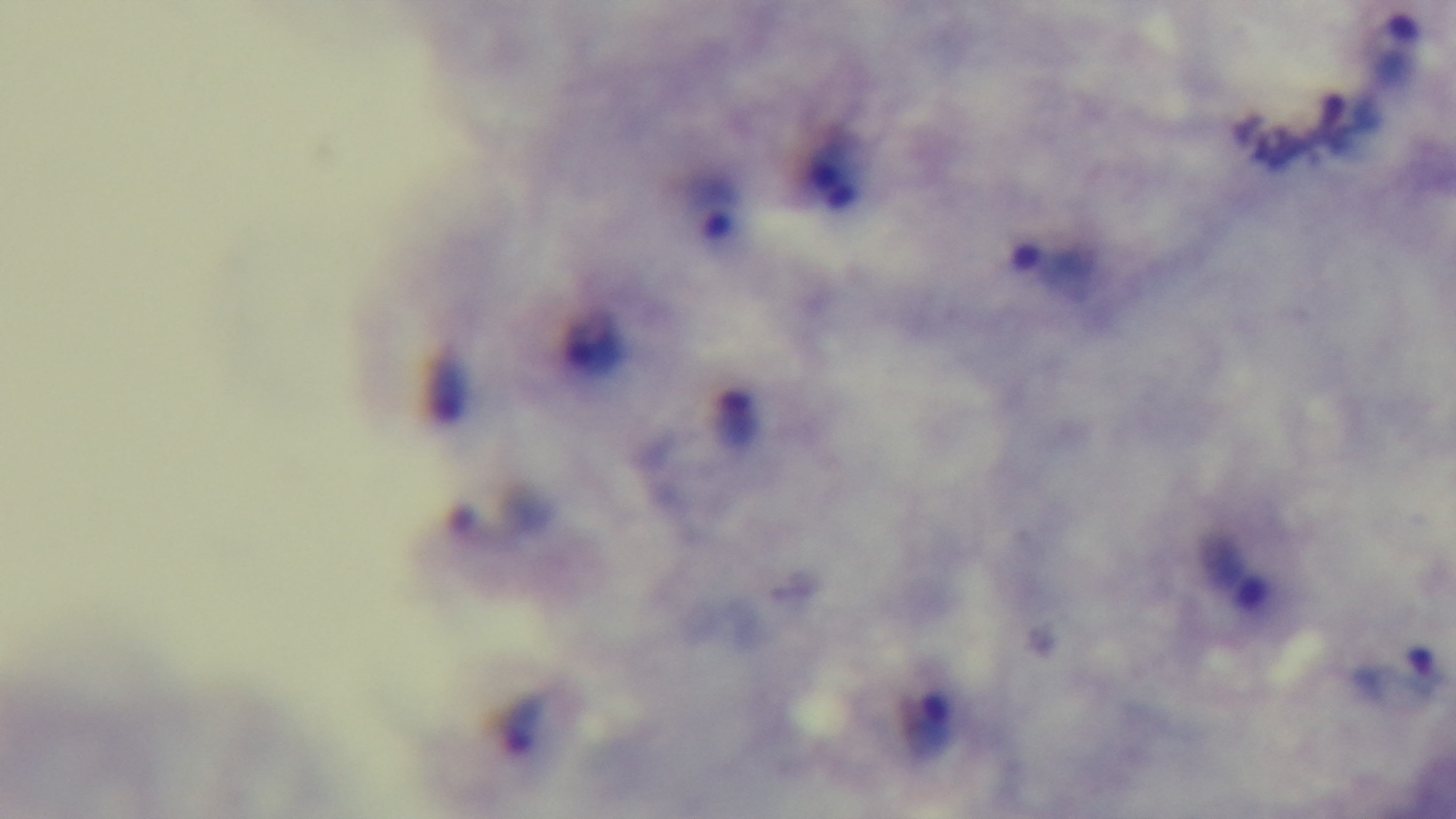
{
  "malaria_status": "infected",
  "stain": "Giemsa",
  "modality": "light microscopy",
  "capture": "mounted 4K digital camera",
  "field_of_view": "single",
  "objective": "100x oil immersion",
  "preparation": "thick blood film"
}